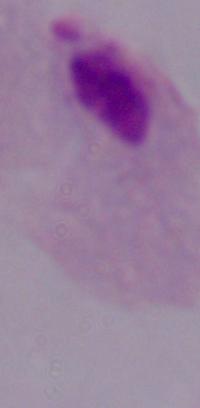

A trichomonad is seen. Micrograph. Captured at 1000x magnification.